Locate every Plasmodium parasite and identify its life-cycle stage.
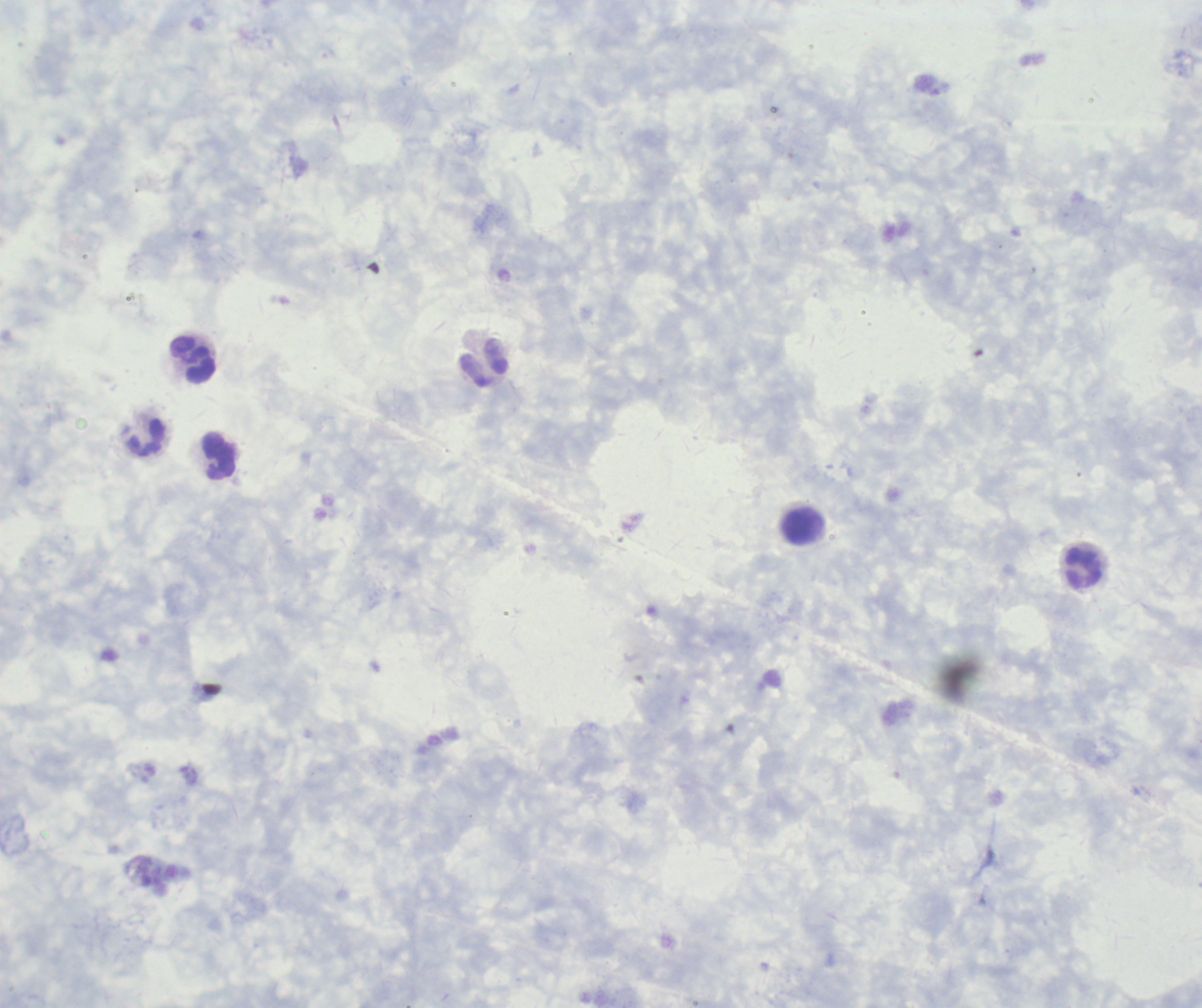

No Plasmodium parasites seen.

coordinate format = approximate object centers, in pixels from the top-left corner
leukocyte locations = (x=193, y=359), (x=484, y=363), (x=147, y=437), (x=217, y=456), (x=803, y=526), (x=1083, y=568)
background quality = poor
field of view = one from this slide
magnification = 100x
preparation = thick smear of blood
coloration quality = good
context = previously used in an actual diagnosis
stain = Romanowsky
image size = 1202×1008 pixels